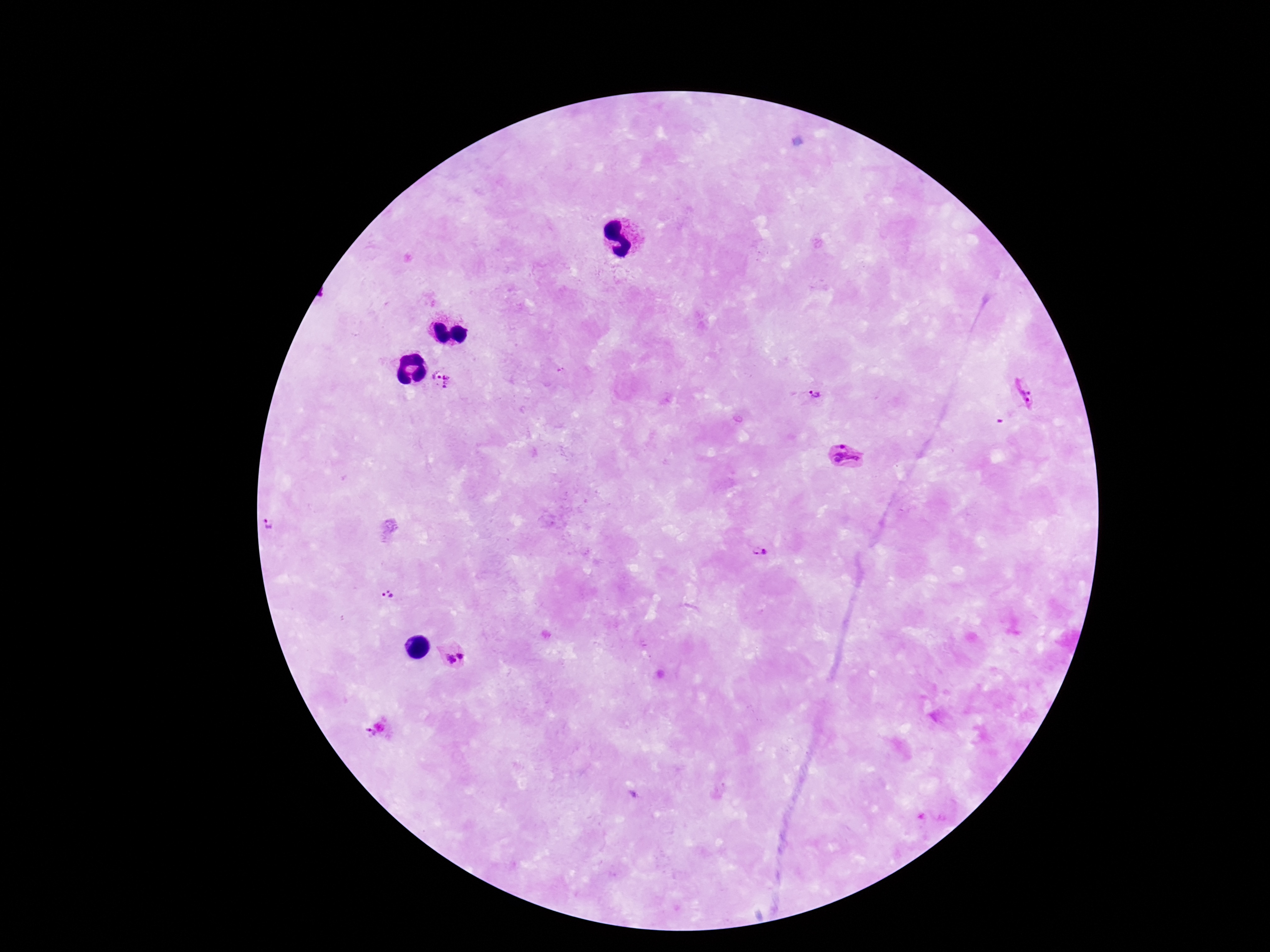

preparation = thick blood film
magnification = 100x
Plasmodium parasite locations = approximate centers as {x, y} in pixels: {443, 380}, {1023, 394}, {818, 395}, {844, 456}, {268, 526}, {760, 553}, {388, 596}, {455, 651}, {369, 732}
patient malaria status = infected
stain = Giemsa
capture = smartphone camera through the microscope eyepiece
image size = 1270×952 pixels
field of view = one from this slide